Outline each uninfected red blood cell.
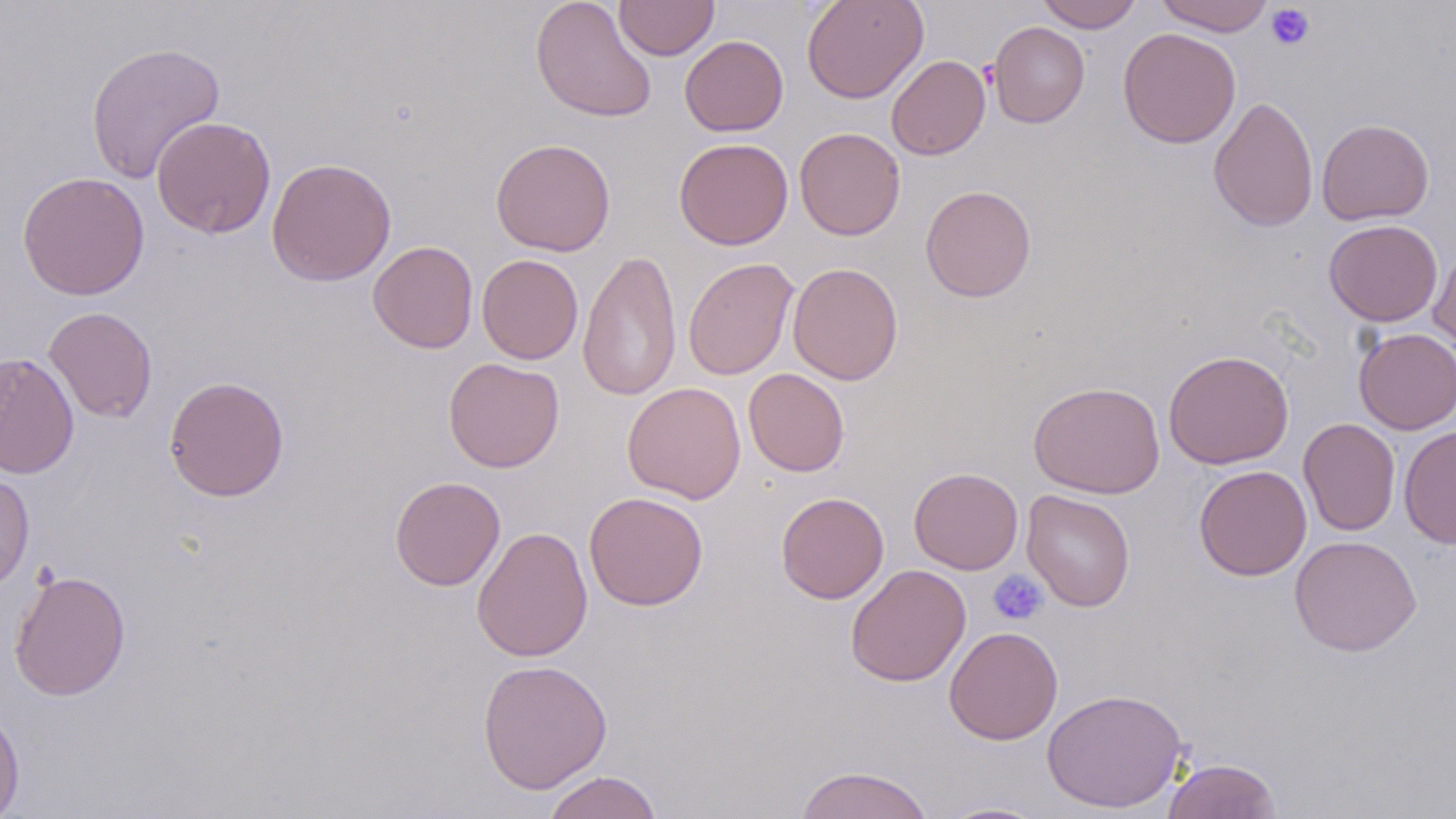
Approximate bounding boxes as (x1,y1)-(x2,y2) corner pairs in pixels.
Uninfected red blood cells: (530,0)-(657,123), (614,0)-(719,61), (801,0)-(928,103), (1035,0)-(1143,32), (1155,0)-(1274,36), (989,21)-(1089,128), (1117,27)-(1240,148), (680,35)-(788,137), (85,41)-(225,184), (887,55)-(990,160), (1209,95)-(1318,232), (151,116)-(276,238), (1317,118)-(1434,225), (794,126)-(905,240), (674,137)-(793,250), (490,138)-(615,256), (266,157)-(396,287), (16,171)-(150,300), (920,185)-(1037,302), (1324,219)-(1442,327), (368,241)-(478,353), (1428,243)-(1456,361), (577,249)-(682,402), (477,254)-(584,364), (682,257)-(799,380), (787,262)-(904,385), (43,306)-(158,422), (1354,327)-(1456,434), (1163,349)-(1294,469), (0,351)-(79,479), (444,357)-(564,473), (743,368)-(850,477), (164,375)-(290,502), (1028,380)-(1165,499), (623,382)-(746,504), (1298,418)-(1400,536), (1398,425)-(1456,549), (1194,465)-(1311,581), (909,467)-(1023,574), (0,470)-(35,597), (390,476)-(505,591), (1022,489)-(1135,612), (776,491)-(889,603), (584,492)-(708,611), (472,526)-(593,662), (1289,535)-(1422,656), (845,564)-(971,687), (9,568)-(131,701), (944,626)-(1063,744), (476,658)-(613,794), (1040,687)-(1189,814), (0,703)-(25,818), (1162,757)-(1282,819), (793,764)-(936,819), (542,770)-(663,819), (937,801)-(1052,818).

Platelet locations: (1265,4)-(1315,51), (988,569)-(1049,626). Slide-level diagnosis: negative for blood parasites. Thin blood film. Single field of view. May-Grünwald-Giemsa stain. Image is 1456×819 pixels. Optical microscopy. 1000x magnification.